Give the extent of all Plasmodium parasites.
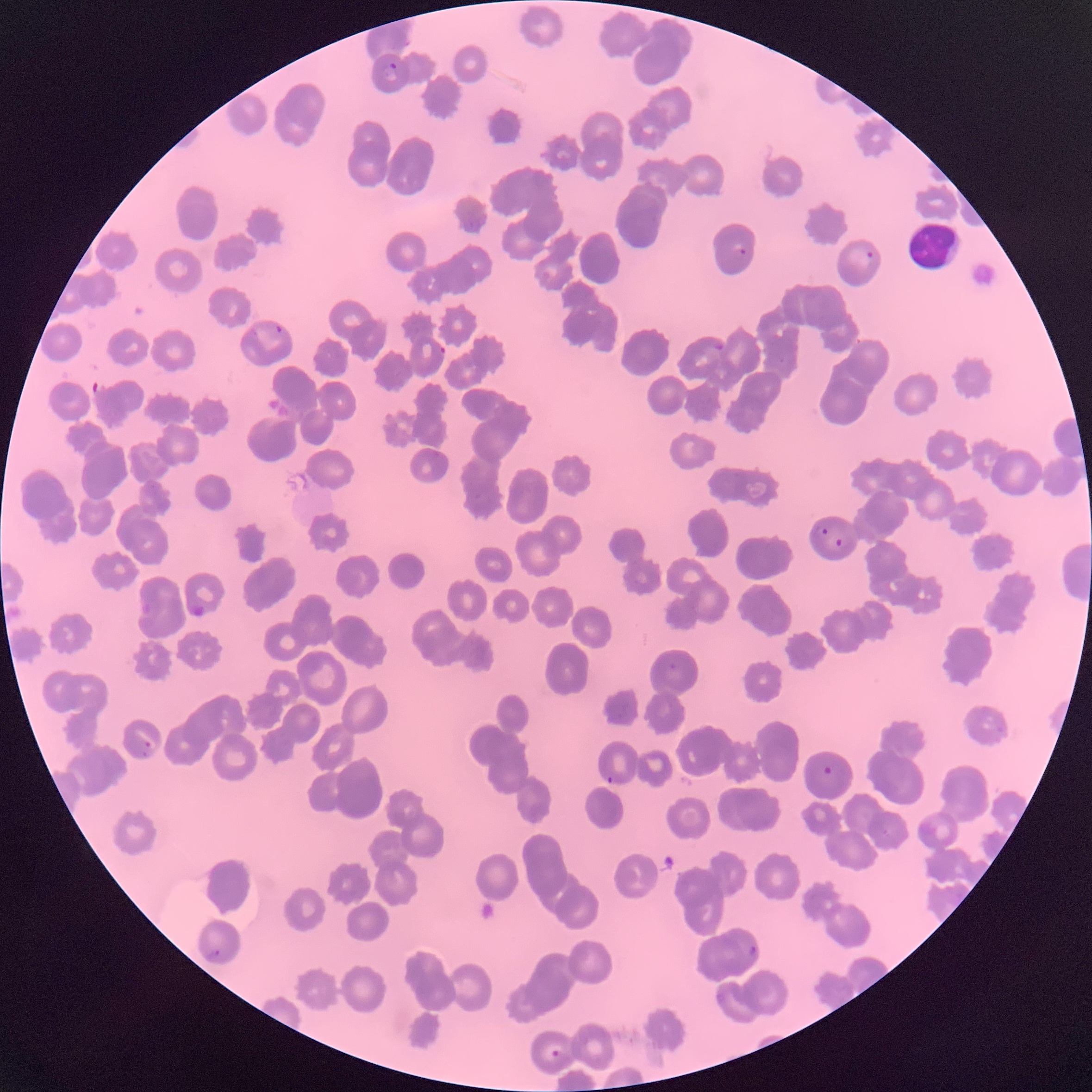

Approximate bounding boxes as (x1,y1)-(x2,y2) corner pairs in pixels.
Plasmodium parasites: (382,62)-(399,82), (738,248)-(748,257), (866,251)-(874,260), (274,323)-(285,334), (713,342)-(724,352), (438,345)-(446,356), (816,524)-(827,535), (835,535)-(852,548), (192,604)-(205,618), (141,741)-(153,759), (822,765)-(833,777), (606,775)-(615,786), (746,945)-(758,962), (207,948)-(221,960), (550,1050)-(561,1058).

Summary:
  - White blood cell locations: (906,222)-(962,271)
  - Preparation: thin blood film
  - Image size: 1092×1092 pixels
  - Modality: optical microscopy
  - Red blood cell morphology: rouleaux formation